Assess this cell for malaria.
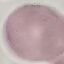

Uninfected.

Summary:
  - Stain: Giemsa
  - Preparation: thin blood film
  - Capture: smartphone through the microscope eyepiece
  - Image type: automatically extracted cell patch, resized to 64 × 64 pixels